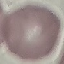

malaria status = uninfected
image type = automatically extracted cell patch, resized to 64 × 64 pixels
stain = Giemsa
capture = smartphone camera at the microscope eyepiece
preparation = thin smear